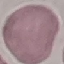
Summary:
  - Malaria status: uninfected
  - Stain: Giemsa
  - Preparation: thin blood film
  - Image type: automatically extracted cell patch, resized to 64 × 64 pixels
  - Capture: smartphone camera at the microscope eyepiece